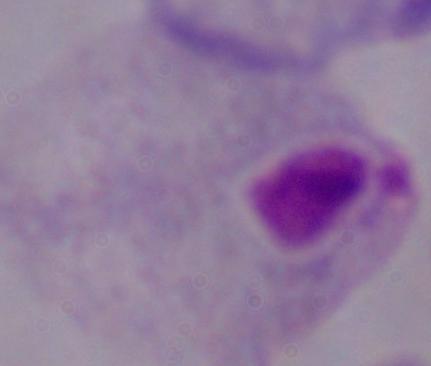 Captured at 1000x magnification. Photomicrograph. A trichomonad is shown.